Identify the blood parasite species.
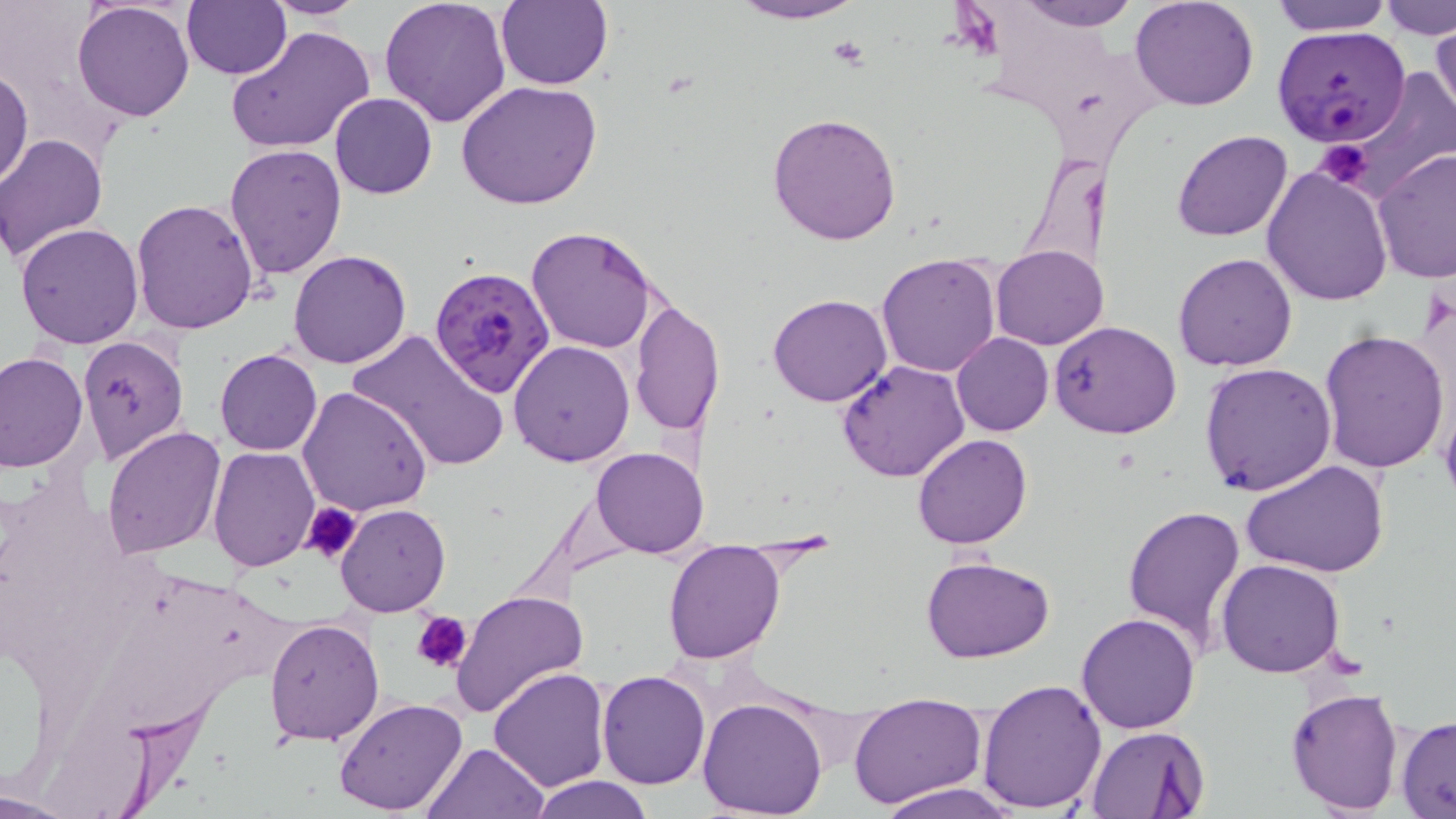
Plasmodium falciparum.

Summary:
  - Coordinate format: approximate bounding boxes as named x1/y1/x2/y2 corners in pixels
  - Plasmodium falciparum-infected red blood cell locations: (x1=1272, y1=26, x2=1411, y2=145), (x1=429, y1=264, x2=559, y2=399)
  - Uninfected red blood cell locations: (x1=181, y1=0, x2=291, y2=80), (x1=261, y1=0, x2=372, y2=21), (x1=380, y1=0, x2=512, y2=127), (x1=497, y1=0, x2=613, y2=90), (x1=726, y1=0, x2=868, y2=25), (x1=1009, y1=0, x2=1143, y2=30), (x1=1130, y1=0, x2=1260, y2=111), (x1=1272, y1=0, x2=1393, y2=35), (x1=71, y1=1, x2=196, y2=121), (x1=1381, y1=1, x2=1456, y2=40), (x1=1428, y1=21, x2=1455, y2=124), (x1=226, y1=24, x2=375, y2=155), (x1=0, y1=66, x2=33, y2=192), (x1=1341, y1=69, x2=1456, y2=198), (x1=458, y1=81, x2=603, y2=210), (x1=329, y1=92, x2=438, y2=199), (x1=767, y1=112, x2=903, y2=247), (x1=1171, y1=130, x2=1292, y2=243), (x1=0, y1=133, x2=110, y2=265), (x1=224, y1=144, x2=348, y2=282), (x1=1372, y1=149, x2=1456, y2=283), (x1=1262, y1=163, x2=1393, y2=306), (x1=131, y1=199, x2=261, y2=337), (x1=16, y1=223, x2=144, y2=349), (x1=526, y1=228, x2=658, y2=352), (x1=991, y1=245, x2=1107, y2=349), (x1=288, y1=249, x2=413, y2=368), (x1=876, y1=251, x2=1002, y2=376), (x1=1171, y1=253, x2=1298, y2=372), (x1=768, y1=292, x2=892, y2=408), (x1=631, y1=302, x2=725, y2=436), (x1=1050, y1=320, x2=1183, y2=439), (x1=347, y1=329, x2=510, y2=475), (x1=1318, y1=330, x2=1451, y2=474), (x1=951, y1=332, x2=1053, y2=437), (x1=76, y1=336, x2=189, y2=469), (x1=509, y1=340, x2=636, y2=466), (x1=215, y1=349, x2=322, y2=456), (x1=0, y1=353, x2=88, y2=473), (x1=835, y1=359, x2=970, y2=482), (x1=1198, y1=363, x2=1337, y2=498), (x1=297, y1=385, x2=433, y2=518), (x1=102, y1=425, x2=228, y2=560), (x1=912, y1=433, x2=1033, y2=549), (x1=207, y1=445, x2=319, y2=572), (x1=592, y1=447, x2=708, y2=558), (x1=1241, y1=458, x2=1389, y2=580), (x1=336, y1=503, x2=451, y2=618), (x1=1120, y1=503, x2=1247, y2=654), (x1=662, y1=540, x2=785, y2=664), (x1=921, y1=555, x2=1055, y2=663), (x1=1217, y1=560, x2=1347, y2=679), (x1=450, y1=590, x2=590, y2=720), (x1=1076, y1=612, x2=1202, y2=734), (x1=262, y1=616, x2=384, y2=745), (x1=489, y1=667, x2=611, y2=792), (x1=596, y1=671, x2=710, y2=790), (x1=977, y1=677, x2=1107, y2=813), (x1=1285, y1=686, x2=1403, y2=814), (x1=848, y1=691, x2=988, y2=808), (x1=698, y1=695, x2=829, y2=819), (x1=333, y1=697, x2=468, y2=816), (x1=1397, y1=716, x2=1456, y2=815), (x1=1084, y1=726, x2=1209, y2=817), (x1=422, y1=742, x2=547, y2=819), (x1=530, y1=776, x2=654, y2=819), (x1=875, y1=782, x2=1019, y2=819), (x1=0, y1=788, x2=80, y2=818)
  - Platelet locations: (x1=1317, y1=141, x2=1372, y2=190), (x1=303, y1=500, x2=361, y2=562), (x1=412, y1=608, x2=472, y2=673)
  - Magnification: 1000x
  - Field of view: single
  - Modality: light microscopy
  - Stain: May-Grünwald-Giemsa
  - Image size: 1456×819 pixels
  - Preparation: thin blood film